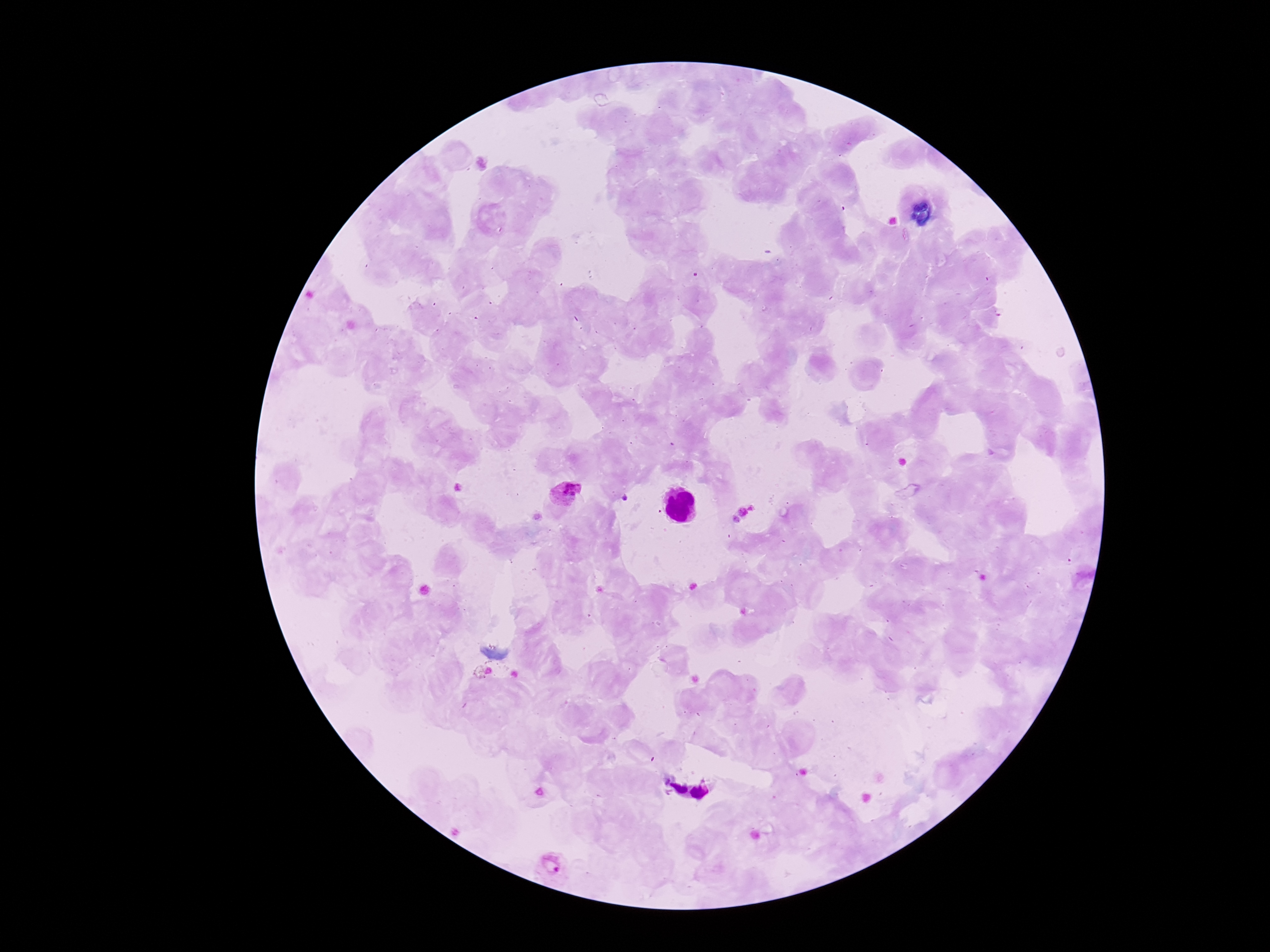

Plasmodium parasite locations = approximate object centers, in pixels from the top-left corner: (x=564, y=493), (x=552, y=866)
magnification = 100x
patient malaria status = positive
field of view = one from this slide
stain = Giemsa
preparation = thick peripheral-blood smear
image size = 1270×952 pixels
capture = smartphone camera through the microscope eyepiece